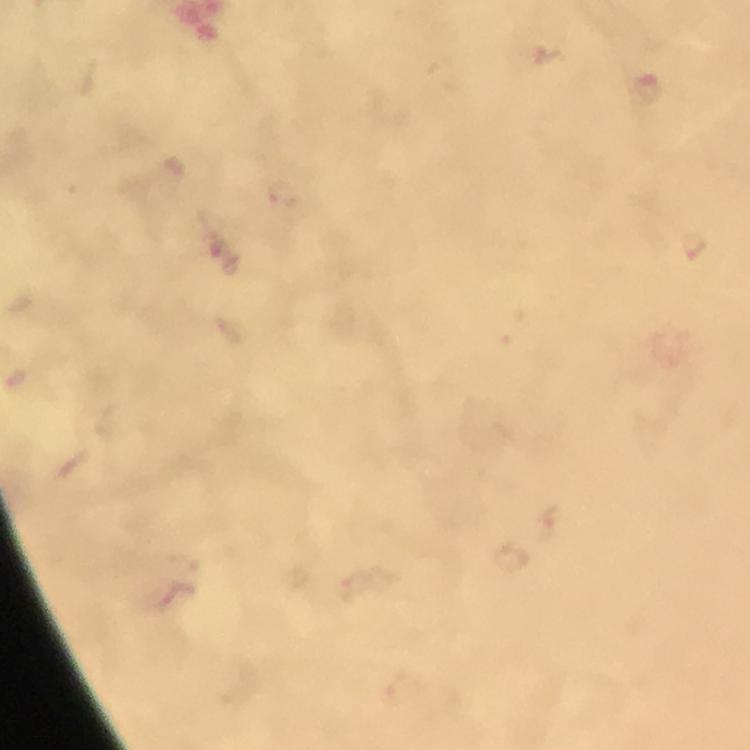

{
  "immersion_oil": "used",
  "magnification": "100x",
  "context": "from a diagnostic examination for malaria",
  "stain": "Giemsa",
  "cropped_from": "a single field of view",
  "capture": "smartphone mounted on the microscope",
  "image_size": "750×750 pixels",
  "preparation": "thick blood smear",
  "malaria_parasite_locations": "approximate centers as {x, y} in pixels: {644, 89}, {694, 248}"
}